Assess the morphology of the red blood cells.
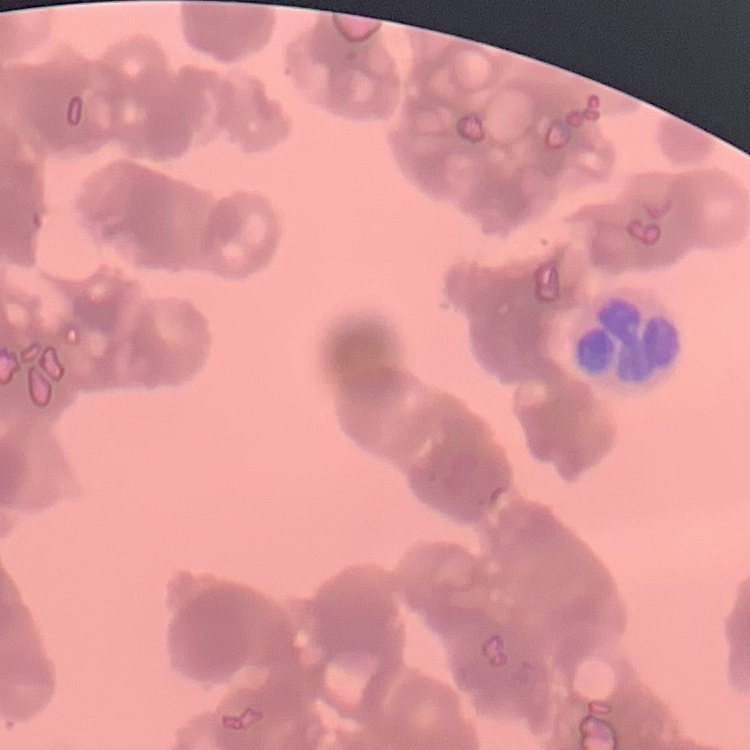
They show rouleaux formation.

Summary:
  - Image type: one tile cut from a larger photomicrograph
  - Stain: Field's or Giemsa
  - Preparation: thin peripheral smear